Comment on the morphology of the erythrocytes.
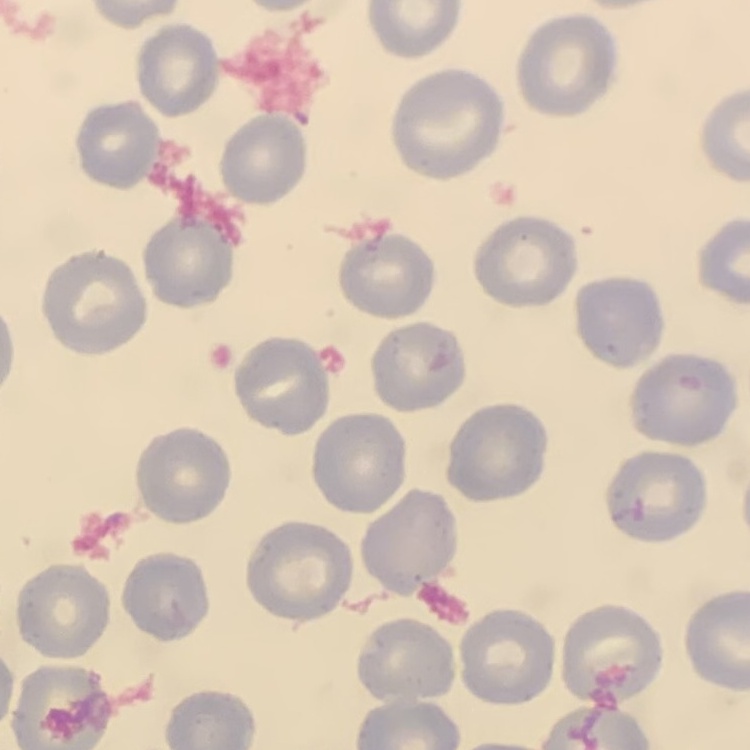

They show no rouleaux formation.

One tile cut from a larger photomicrograph. Thin peripheral smear. Stained with either Field's or Giemsa.